Locate every Plasmodium ovale-infected red blood cell.
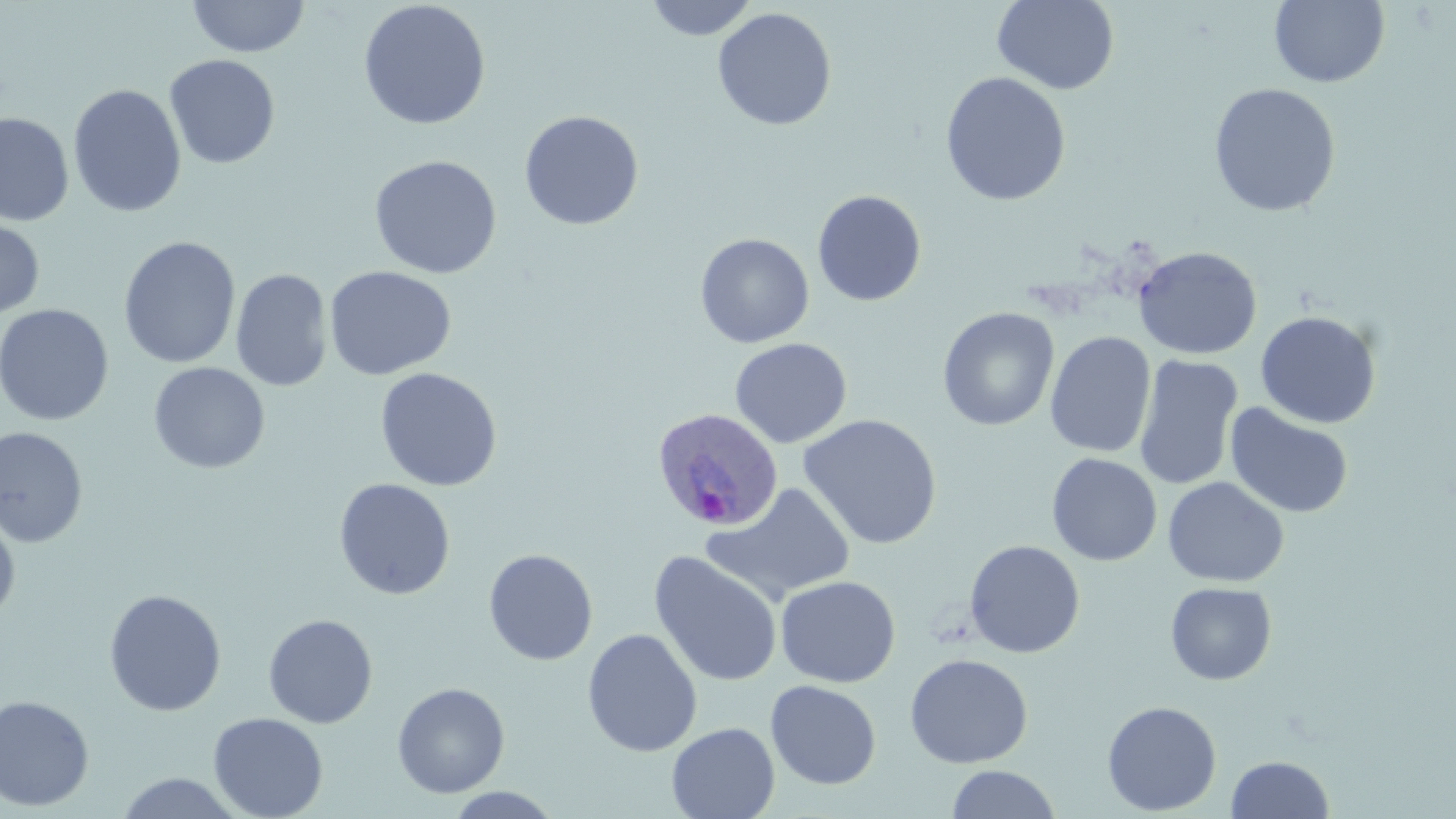
Approximate bounding boxes as named x1/y1/x2/y2 corners in pixels.
Plasmodium ovale-infected red blood cells: (x1=650, y1=406, x2=782, y2=532).

slide-level diagnosis = Plasmodium ovale
stain = May-Grünwald-Giemsa
modality = optical microscopy
preparation = thin blood film
uninfected red blood cell locations = approximate bounding boxes as named x1/y1/x2/y2 corners in pixels: (x1=186, y1=0, x2=310, y2=58), (x1=358, y1=0, x2=491, y2=130), (x1=645, y1=0, x2=758, y2=41), (x1=992, y1=0, x2=1120, y2=95), (x1=1269, y1=0, x2=1390, y2=89), (x1=713, y1=7, x2=837, y2=131), (x1=165, y1=54, x2=280, y2=169), (x1=939, y1=71, x2=1071, y2=207), (x1=1208, y1=82, x2=1341, y2=217), (x1=68, y1=83, x2=187, y2=218), (x1=519, y1=110, x2=644, y2=231), (x1=0, y1=112, x2=75, y2=226), (x1=368, y1=154, x2=503, y2=279), (x1=811, y1=189, x2=927, y2=306), (x1=0, y1=216, x2=45, y2=320), (x1=695, y1=232, x2=815, y2=349), (x1=118, y1=236, x2=240, y2=369), (x1=1133, y1=245, x2=1263, y2=360), (x1=324, y1=266, x2=456, y2=380), (x1=231, y1=268, x2=333, y2=391), (x1=0, y1=303, x2=115, y2=426), (x1=937, y1=307, x2=1059, y2=430), (x1=1255, y1=310, x2=1382, y2=429), (x1=1044, y1=330, x2=1156, y2=458), (x1=729, y1=337, x2=852, y2=449), (x1=1133, y1=354, x2=1244, y2=492), (x1=148, y1=362, x2=271, y2=474), (x1=374, y1=367, x2=502, y2=491), (x1=1224, y1=403, x2=1354, y2=519), (x1=798, y1=414, x2=942, y2=550), (x1=0, y1=426, x2=89, y2=548), (x1=1046, y1=453, x2=1162, y2=566), (x1=1163, y1=476, x2=1289, y2=587), (x1=333, y1=478, x2=456, y2=600), (x1=701, y1=482, x2=856, y2=606), (x1=0, y1=511, x2=21, y2=625), (x1=964, y1=539, x2=1085, y2=658), (x1=482, y1=549, x2=598, y2=666), (x1=649, y1=551, x2=783, y2=687), (x1=775, y1=575, x2=900, y2=688), (x1=1165, y1=581, x2=1278, y2=685), (x1=103, y1=589, x2=227, y2=716), (x1=263, y1=613, x2=378, y2=728), (x1=582, y1=628, x2=702, y2=757), (x1=904, y1=654, x2=1033, y2=768), (x1=765, y1=679, x2=882, y2=789), (x1=391, y1=681, x2=510, y2=798), (x1=0, y1=694, x2=95, y2=811), (x1=1101, y1=700, x2=1222, y2=815), (x1=208, y1=712, x2=329, y2=819), (x1=666, y1=722, x2=779, y2=819), (x1=1225, y1=754, x2=1335, y2=818), (x1=946, y1=765, x2=1062, y2=819), (x1=112, y1=772, x2=249, y2=818), (x1=443, y1=787, x2=566, y2=818)
magnification = 1000x
image size = 1456×819 pixels
field of view = single